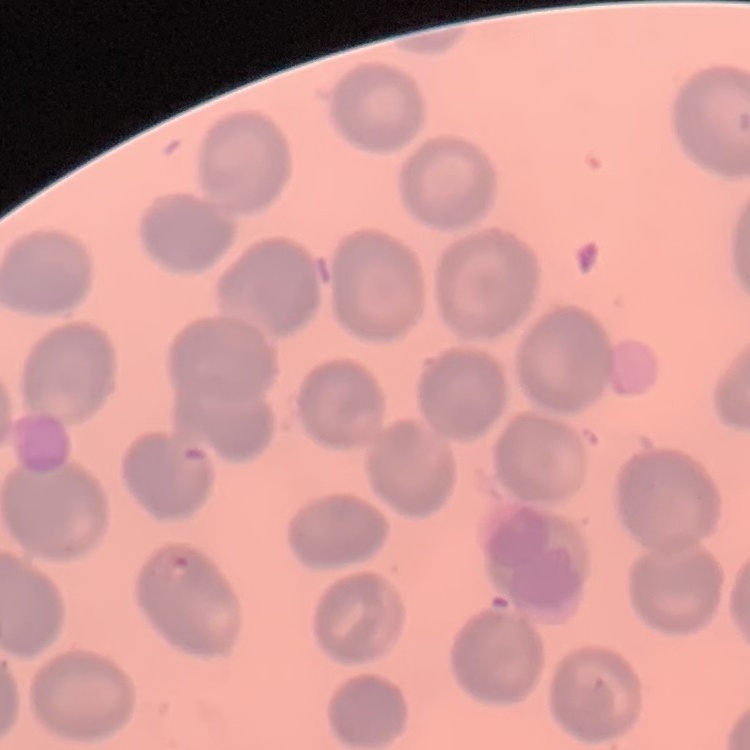
Summary:
  - Red blood cell morphology: no rouleaux formation
  - Image type: one tile cut from a larger photomicrograph
  - Stain: Field's or Giemsa
  - Preparation: thin blood film